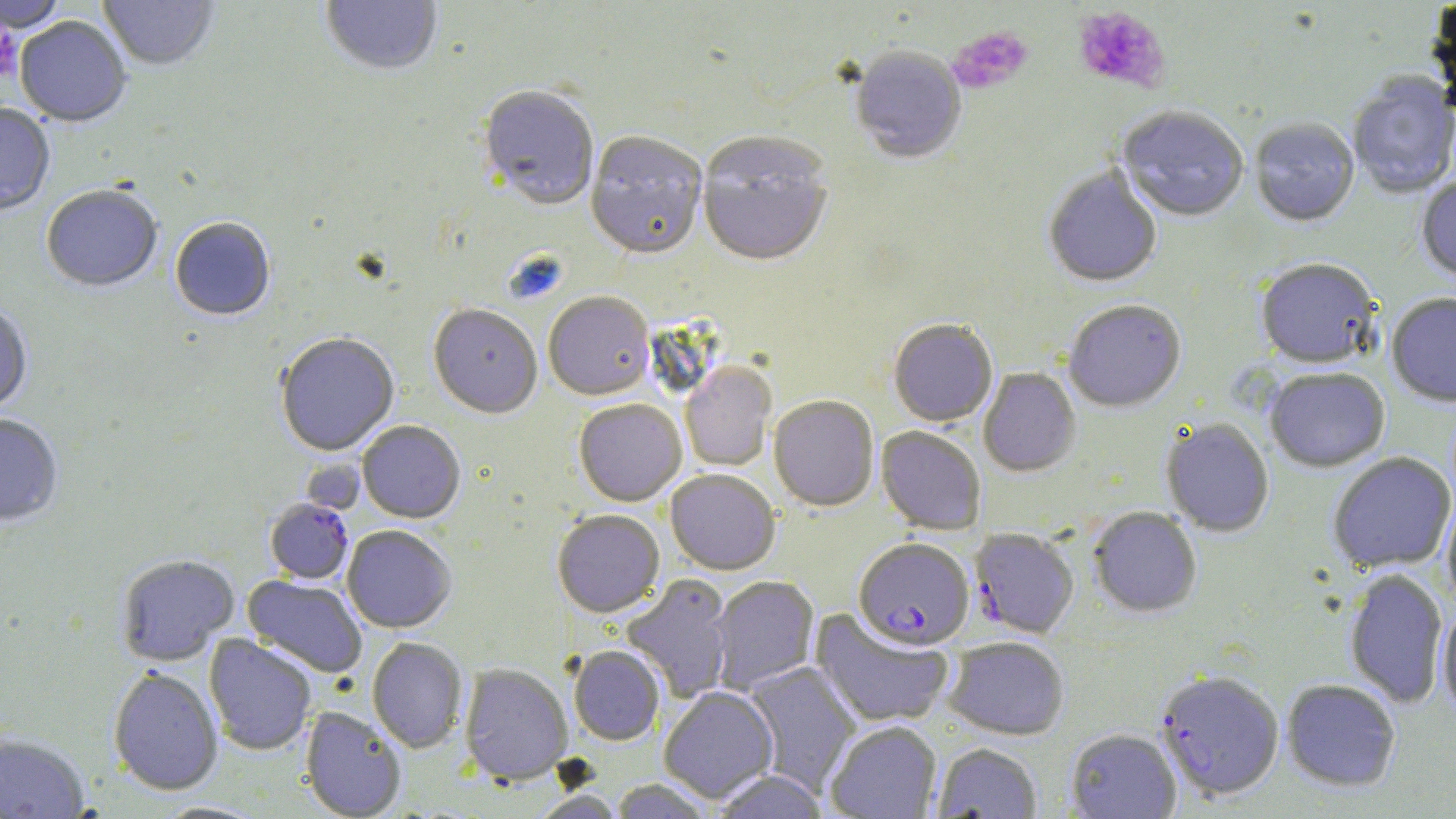

Approximate bounding boxes as (x1,y1)-(x2,y2) corner pairs in pixels. Plasmodium falciparum-infected red blood cell locations: (265,499)-(353,585), (969,528)-(1079,639), (854,539)-(974,651), (1155,671)-(1284,803). Platelet locations: (1072,6)-(1169,94), (0,23)-(22,83), (948,26)-(1033,94). Uninfected red blood cell locations: (1,0)-(67,34), (99,0)-(219,73), (320,0)-(442,77), (1427,0)-(1456,110), (14,18)-(131,129), (849,48)-(966,166), (1348,74)-(1456,200), (478,88)-(599,213), (0,105)-(55,217), (1117,108)-(1249,224), (1250,119)-(1360,229), (585,134)-(708,262), (697,135)-(834,271), (1043,166)-(1162,289), (1416,177)-(1456,284), (41,187)-(162,294), (170,219)-(275,322), (1255,260)-(1381,370), (543,294)-(655,402), (1387,294)-(1456,409), (1063,301)-(1186,413), (0,305)-(33,416), (428,306)-(542,420), (888,320)-(998,428), (275,334)-(399,457), (680,362)-(777,471), (978,368)-(1081,478), (1265,369)-(1389,473), (768,396)-(879,512), (574,400)-(687,507), (0,415)-(63,527), (1160,419)-(1274,537), (357,422)-(465,524), (876,426)-(986,535), (1328,453)-(1455,574), (665,470)-(779,576), (1442,495)-(1456,609), (1088,508)-(1202,618), (552,511)-(665,618), (342,526)-(456,634), (116,555)-(239,666), (1344,569)-(1448,708), (242,575)-(368,679), (622,576)-(735,703), (709,576)-(820,695), (1437,605)-(1456,720), (810,608)-(954,728), (204,634)-(316,756), (944,637)-(1069,741), (367,638)-(468,753), (568,646)-(664,746), (743,661)-(861,795), (459,664)-(573,786), (108,667)-(223,797), (1281,679)-(1401,793), (659,688)-(778,804), (300,706)-(406,819), (825,722)-(941,819), (1065,729)-(1182,818), (0,734)-(90,818), (932,743)-(1042,818), (711,770)-(829,819), (609,779)-(713,819), (529,791)-(624,819). Slide-level diagnosis: Plasmodium falciparum. Image is 1456×819 pixels. May-Grünwald-Giemsa-stained preparation. One field of a larger specimen. Light microscopy. 1000x magnification. Thin blood smear.